State the blood parasite species.
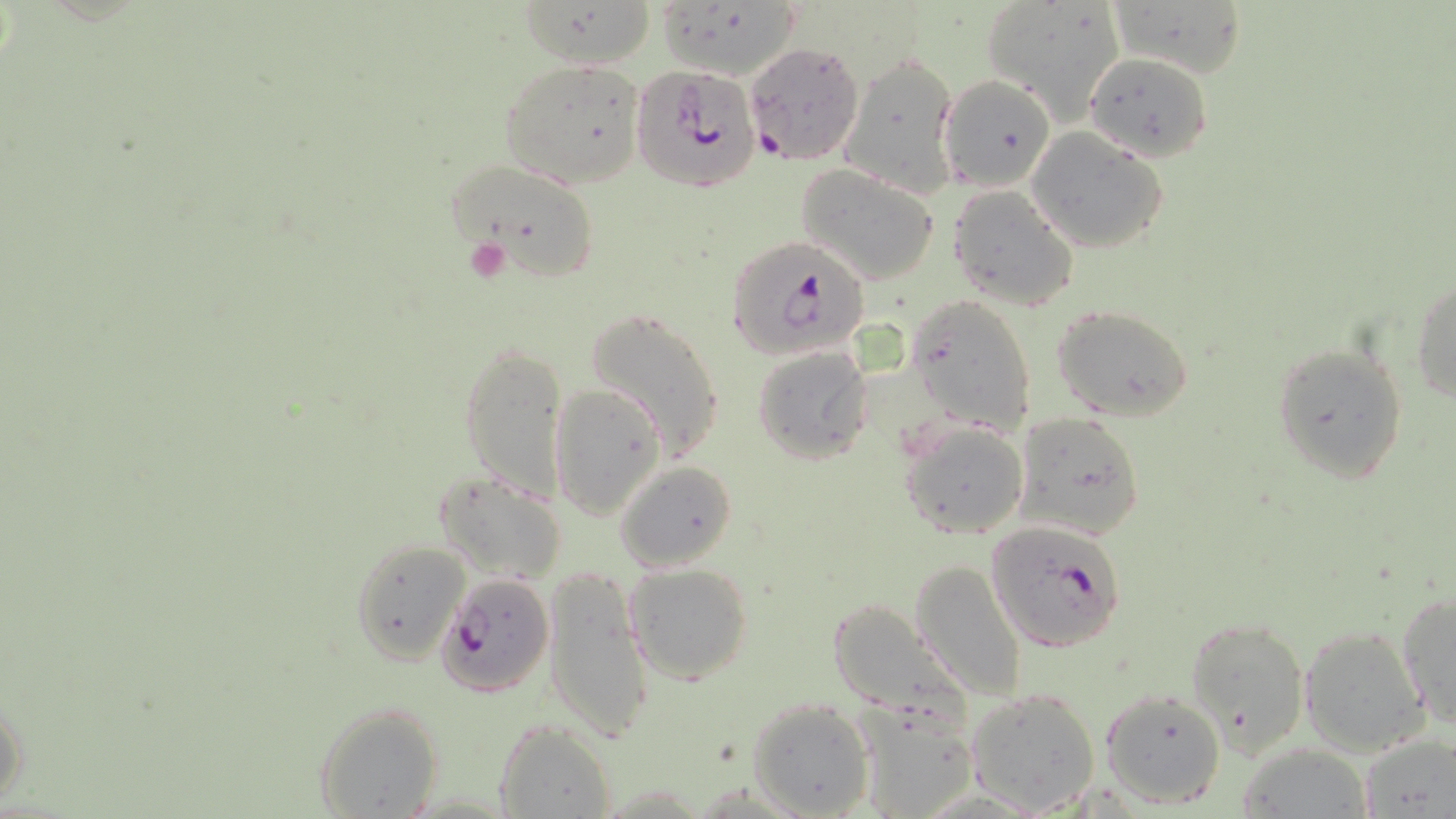
Plasmodium falciparum.

field of view = single
Plasmodium falciparum-infected red blood cell locations = approximate bounding boxes as (x1, y1, x2, y2) in pixels: (743, 39, 864, 166), (633, 62, 761, 192), (727, 237, 868, 358), (985, 518, 1131, 654), (437, 572, 555, 698)
platelet locations = approximate bounding boxes as (x1, y1, x2, y2) in pixels: (463, 237, 512, 284)
uninfected red blood cell locations = approximate bounding boxes as (x1, y1, x2, y2) in pixels: (979, 0, 1124, 118), (1109, 0, 1247, 81), (519, 2, 659, 70), (842, 53, 960, 198), (1084, 53, 1213, 162), (499, 59, 646, 188), (941, 73, 1055, 192), (1026, 127, 1171, 254), (450, 159, 600, 280), (796, 164, 941, 286), (947, 186, 1079, 313), (1411, 280, 1456, 403), (907, 293, 1036, 438), (584, 306, 727, 463), (1053, 306, 1195, 423), (460, 338, 568, 502), (1270, 342, 1409, 483), (752, 346, 873, 464), (551, 381, 666, 520), (1015, 411, 1142, 540), (899, 418, 1030, 540), (615, 460, 740, 573), (433, 471, 567, 584), (349, 538, 471, 667), (909, 559, 1028, 700), (623, 562, 753, 685), (543, 565, 653, 741), (1397, 590, 1456, 726), (824, 597, 970, 726), (1188, 616, 1309, 753), (1300, 625, 1430, 756), (965, 685, 1102, 813), (1098, 687, 1227, 808), (0, 693, 27, 808), (747, 697, 874, 818), (313, 700, 444, 817), (851, 701, 977, 817), (493, 719, 615, 819), (1357, 732, 1454, 816), (1237, 744, 1373, 817)
magnification = 1000x
stain = May-Grünwald-Giemsa
image size = 1456×819 pixels
preparation = thin blood film
modality = light microscopy